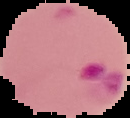

image_type: segmented cell region on a black background
image_size: 130×118 pixels
preparation: thin blood film
malaria_status: parasitized